Describe the morphology of the red blood cells.
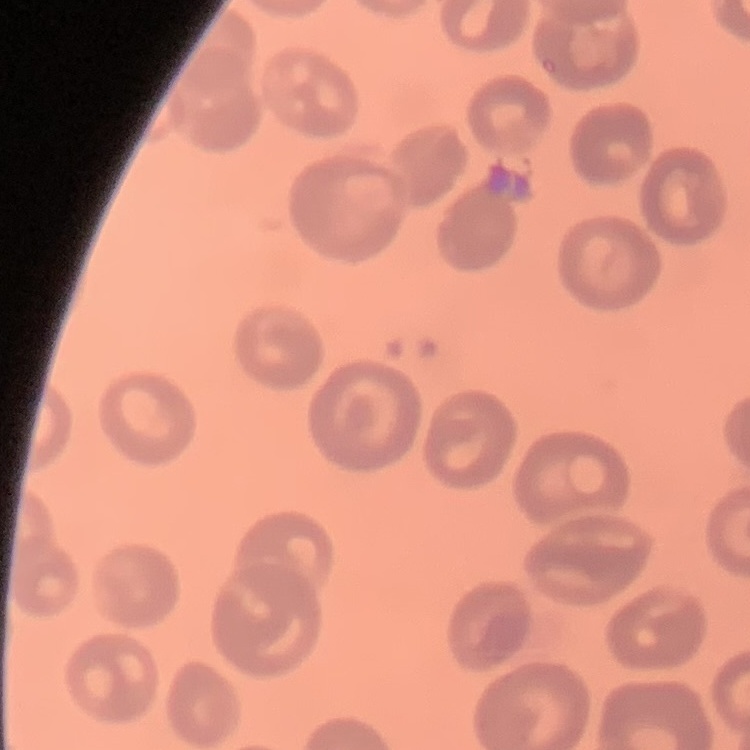
They show no rouleaux formation.

Square crop of a larger photomicrograph. Field's or Giemsa stain. Thin peripheral smear.